Locate every malaria parasite.
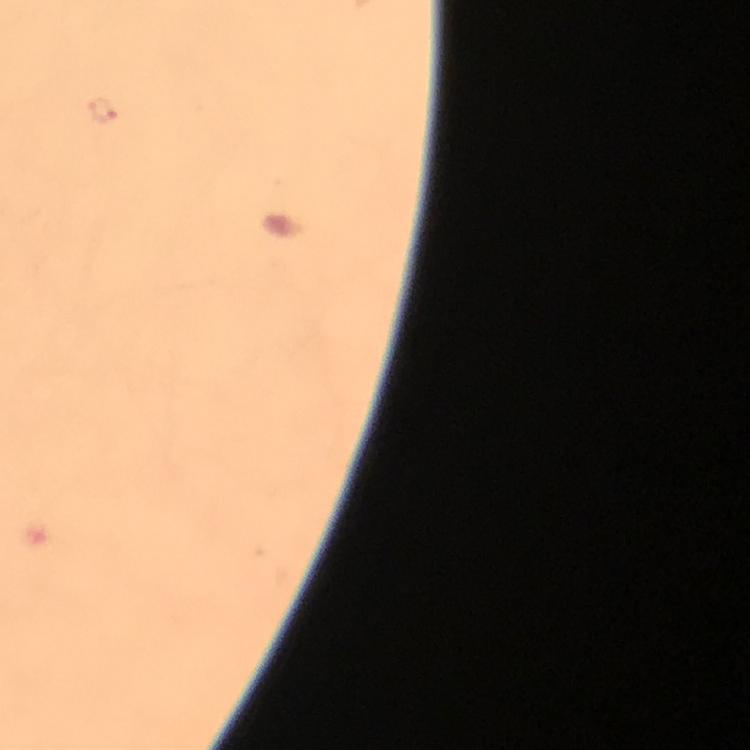

Approximate centers as (x, y) in pixels.
Malaria parasites: (100, 108).

context = from a malaria diagnostic workup
image size = 750×750 pixels
immersion oil = applied
magnification = 100x
stain = Giemsa
capture = smartphone camera through the microscope
cropped from = one field of view
preparation = thick blood smear